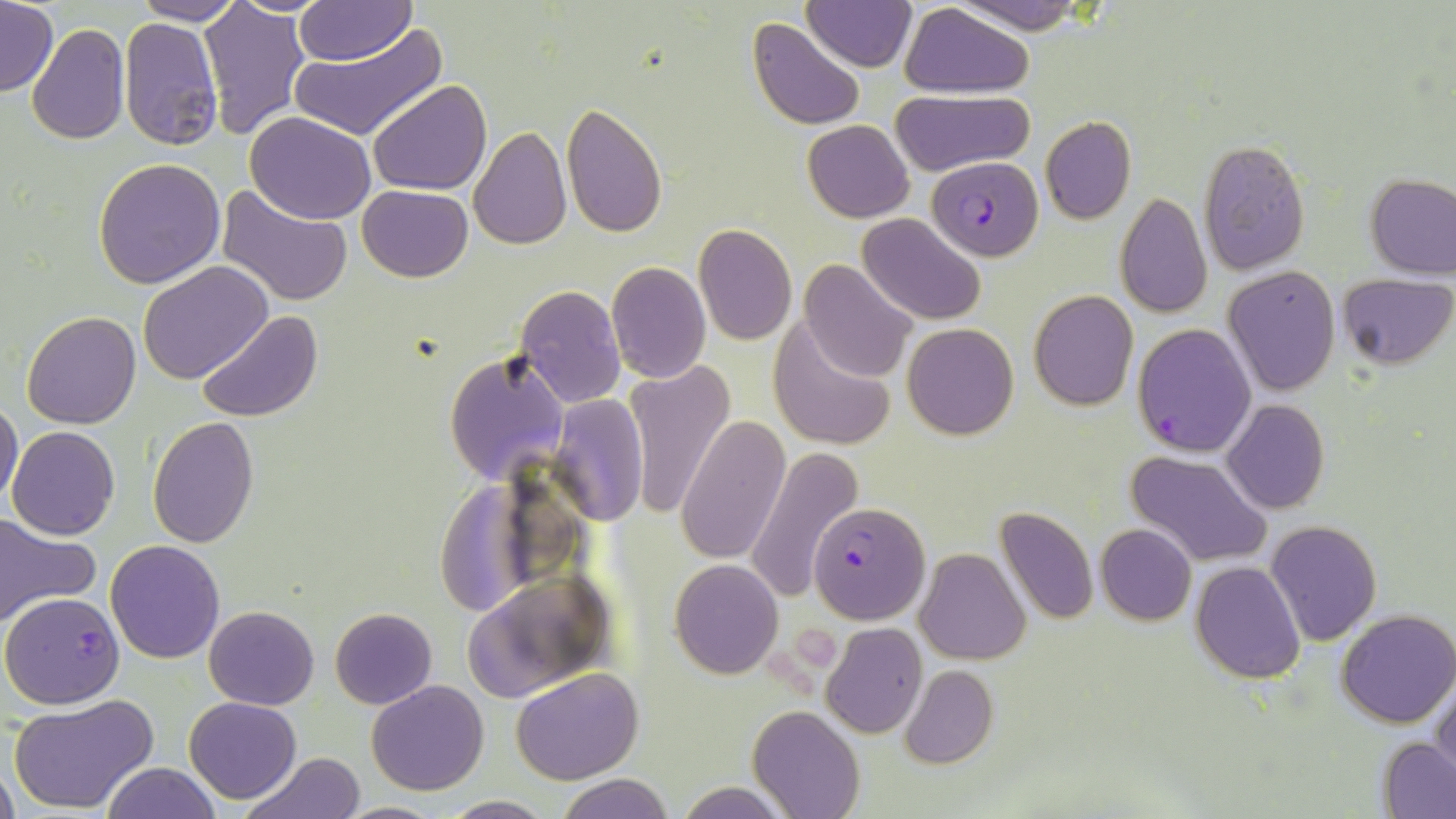

Approximate bounding boxes as named x1/y1/x2/y2 corners in pixels. Plasmodium falciparum-infected red blood cell locations: (x1=927, y1=156, x2=1044, y2=260), (x1=1131, y1=324, x2=1256, y2=457), (x1=809, y1=501, x2=931, y2=625), (x1=0, y1=591, x2=126, y2=710). Uninfected red blood cell locations: (x1=130, y1=0, x2=245, y2=24), (x1=952, y1=0, x2=1089, y2=35), (x1=0, y1=1, x2=58, y2=97), (x1=198, y1=1, x2=310, y2=138), (x1=295, y1=1, x2=416, y2=66), (x1=804, y1=1, x2=915, y2=71), (x1=901, y1=4, x2=1033, y2=96), (x1=119, y1=17, x2=223, y2=149), (x1=748, y1=18, x2=866, y2=131), (x1=27, y1=24, x2=130, y2=145), (x1=287, y1=25, x2=444, y2=142), (x1=368, y1=80, x2=492, y2=197), (x1=892, y1=90, x2=1033, y2=177), (x1=560, y1=105, x2=668, y2=239), (x1=245, y1=112, x2=376, y2=223), (x1=1040, y1=115, x2=1136, y2=224), (x1=803, y1=119, x2=914, y2=222), (x1=469, y1=126, x2=572, y2=248), (x1=1198, y1=141, x2=1311, y2=275), (x1=93, y1=157, x2=225, y2=287), (x1=1365, y1=173, x2=1455, y2=278), (x1=356, y1=184, x2=473, y2=282), (x1=218, y1=186, x2=352, y2=306), (x1=1114, y1=191, x2=1211, y2=319), (x1=858, y1=213, x2=986, y2=325), (x1=692, y1=224, x2=798, y2=346), (x1=799, y1=259, x2=917, y2=382), (x1=138, y1=260, x2=274, y2=385), (x1=606, y1=260, x2=711, y2=384), (x1=1224, y1=266, x2=1341, y2=397), (x1=1336, y1=274, x2=1453, y2=369), (x1=514, y1=284, x2=625, y2=407), (x1=1028, y1=291, x2=1138, y2=410), (x1=197, y1=310, x2=325, y2=425), (x1=22, y1=311, x2=142, y2=428), (x1=766, y1=318, x2=898, y2=453), (x1=902, y1=322, x2=1018, y2=439), (x1=443, y1=350, x2=570, y2=488), (x1=624, y1=361, x2=736, y2=519), (x1=548, y1=393, x2=651, y2=525), (x1=0, y1=397, x2=23, y2=510), (x1=1222, y1=400, x2=1330, y2=515), (x1=677, y1=415, x2=790, y2=564), (x1=147, y1=417, x2=259, y2=547), (x1=8, y1=426, x2=121, y2=542), (x1=744, y1=446, x2=863, y2=599), (x1=1125, y1=451, x2=1272, y2=568), (x1=431, y1=477, x2=548, y2=615), (x1=994, y1=506, x2=1099, y2=626), (x1=0, y1=513, x2=99, y2=627), (x1=1265, y1=520, x2=1381, y2=645), (x1=1095, y1=523, x2=1197, y2=625), (x1=105, y1=539, x2=227, y2=663), (x1=916, y1=548, x2=1031, y2=663), (x1=668, y1=559, x2=783, y2=679), (x1=1190, y1=561, x2=1306, y2=684), (x1=461, y1=570, x2=617, y2=704), (x1=205, y1=605, x2=320, y2=710), (x1=329, y1=607, x2=439, y2=710), (x1=1335, y1=608, x2=1456, y2=729), (x1=820, y1=622, x2=929, y2=738), (x1=899, y1=665, x2=999, y2=770), (x1=511, y1=667, x2=644, y2=785), (x1=1431, y1=673, x2=1456, y2=783), (x1=367, y1=680, x2=489, y2=796), (x1=8, y1=693, x2=159, y2=814), (x1=183, y1=695, x2=302, y2=804), (x1=749, y1=705, x2=864, y2=819), (x1=1379, y1=738, x2=1456, y2=817), (x1=242, y1=753, x2=365, y2=819), (x1=101, y1=762, x2=221, y2=819), (x1=1, y1=764, x2=19, y2=819), (x1=555, y1=774, x2=676, y2=819), (x1=676, y1=780, x2=791, y2=818), (x1=441, y1=795, x2=555, y2=817), (x1=331, y1=801, x2=452, y2=819). Platelet locations: (x1=791, y1=625, x2=838, y2=662), (x1=767, y1=647, x2=797, y2=680), (x1=790, y1=673, x2=817, y2=700). Slide-level diagnosis: Plasmodium falciparum. 1000x magnification. Image is 1456×819 pixels. One field of a larger specimen. Thin blood film. Light microscopy. May-Grünwald-Giemsa-stained preparation.